Name the parasite shown.
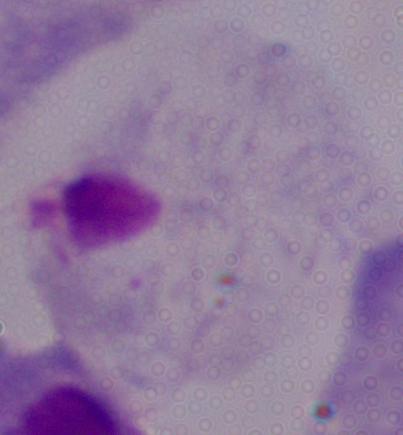

This is a trichomonad.

Micrograph. Captured at 1000x magnification.